Identify the blood parasite species.
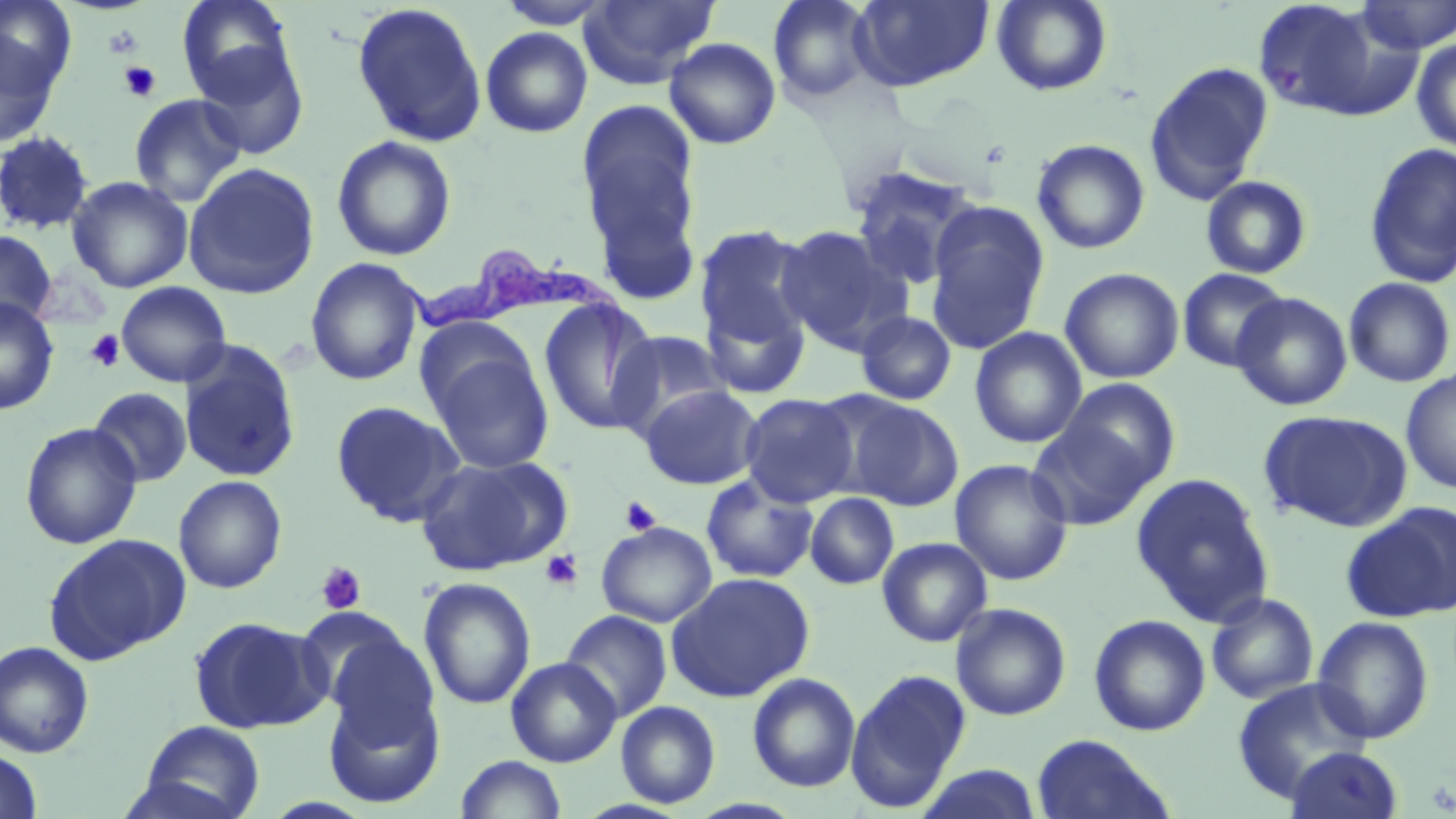
Trypanosoma brucei.

preparation: thin blood film
uninfected_red_blood_cell_locations: 'approximate bounding boxes as named x1/y1/x2/y2 corners in pixels: (x1=0, y1=0, x2=77, y2=95), (x1=177, y1=0, x2=295, y2=101), (x1=496, y1=0, x2=616, y2=28), (x1=579, y1=0, x2=719, y2=89), (x1=768, y1=0, x2=877, y2=104), (x1=850, y1=0, x2=995, y2=92), (x1=991, y1=0, x2=1112, y2=97), (x1=1251, y1=0, x2=1405, y2=122), (x1=1355, y1=0, x2=1456, y2=54), (x1=351, y1=2, x2=488, y2=148), (x1=480, y1=27, x2=593, y2=138), (x1=0, y1=29, x2=61, y2=149), (x1=664, y1=37, x2=781, y2=149), (x1=1411, y1=38, x2=1456, y2=153), (x1=193, y1=42, x2=309, y2=159), (x1=1144, y1=62, x2=1274, y2=204), (x1=128, y1=93, x2=246, y2=207), (x1=575, y1=99, x2=703, y2=273), (x1=0, y1=130, x2=95, y2=236), (x1=331, y1=135, x2=457, y2=262), (x1=1031, y1=139, x2=1150, y2=254), (x1=1363, y1=141, x2=1456, y2=288), (x1=183, y1=163, x2=320, y2=299), (x1=848, y1=165, x2=985, y2=291), (x1=1200, y1=175, x2=1313, y2=279), (x1=66, y1=176, x2=193, y2=293), (x1=924, y1=201, x2=1051, y2=354), (x1=694, y1=222, x2=816, y2=369), (x1=775, y1=224, x2=909, y2=353), (x1=0, y1=230, x2=56, y2=331), (x1=305, y1=257, x2=426, y2=386), (x1=1060, y1=267, x2=1185, y2=384), (x1=1177, y1=268, x2=1289, y2=373), (x1=1343, y1=277, x2=1455, y2=388), (x1=116, y1=281, x2=232, y2=386), (x1=1231, y1=292, x2=1353, y2=411), (x1=0, y1=297, x2=59, y2=415), (x1=537, y1=298, x2=660, y2=436), (x1=856, y1=311, x2=956, y2=406), (x1=970, y1=327, x2=1087, y2=449), (x1=609, y1=330, x2=733, y2=438), (x1=178, y1=340, x2=302, y2=484), (x1=428, y1=348, x2=555, y2=474), (x1=1401, y1=368, x2=1456, y2=493), (x1=1057, y1=379, x2=1180, y2=489), (x1=639, y1=384, x2=763, y2=490), (x1=89, y1=386, x2=193, y2=487), (x1=739, y1=393, x2=859, y2=507), (x1=840, y1=397, x2=964, y2=511), (x1=331, y1=400, x2=465, y2=527), (x1=1258, y1=409, x2=1413, y2=532), (x1=1027, y1=421, x2=1154, y2=531), (x1=20, y1=422, x2=143, y2=549), (x1=415, y1=454, x2=573, y2=576), (x1=950, y1=458, x2=1074, y2=585), (x1=1131, y1=472, x2=1274, y2=626), (x1=700, y1=474, x2=819, y2=584), (x1=172, y1=475, x2=287, y2=594), (x1=805, y1=493, x2=899, y2=590), (x1=1344, y1=502, x2=1456, y2=622), (x1=596, y1=521, x2=718, y2=627), (x1=43, y1=532, x2=191, y2=664), (x1=877, y1=537, x2=992, y2=647), (x1=666, y1=572, x2=814, y2=702), (x1=418, y1=577, x2=537, y2=710), (x1=1206, y1=592, x2=1319, y2=705), (x1=951, y1=603, x2=1071, y2=721), (x1=560, y1=610, x2=673, y2=723), (x1=296, y1=611, x2=428, y2=728), (x1=1088, y1=614, x2=1211, y2=736), (x1=1311, y1=615, x2=1435, y2=744), (x1=188, y1=616, x2=327, y2=733), (x1=0, y1=641, x2=95, y2=758), (x1=506, y1=657, x2=621, y2=768), (x1=322, y1=669, x2=446, y2=810), (x1=845, y1=669, x2=971, y2=811), (x1=747, y1=672, x2=861, y2=792), (x1=1232, y1=678, x2=1373, y2=803), (x1=615, y1=700, x2=721, y2=808), (x1=138, y1=720, x2=265, y2=819), (x1=1031, y1=734, x2=1175, y2=819), (x1=1283, y1=746, x2=1404, y2=819), (x1=0, y1=748, x2=44, y2=817), (x1=455, y1=755, x2=567, y2=819), (x1=914, y1=764, x2=1044, y2=819)'
field_of_view: single
modality: light microscopy
stain: May-Grünwald-Giemsa
magnification: 1000x
platelet_locations: 'approximate bounding boxes as named x1/y1/x2/y2 corners in pixels: (x1=102, y1=23, x2=145, y2=58), (x1=119, y1=60, x2=161, y2=102), (x1=85, y1=330, x2=125, y2=372), (x1=620, y1=496, x2=662, y2=536), (x1=540, y1=550, x2=583, y2=590), (x1=317, y1=562, x2=366, y2=614)'
image_size: 1456×819 pixels
trypanosoma_brucei_locations: 'approximate bounding boxes as named x1/y1/x2/y2 corners in pixels: (x1=398, y1=247, x2=631, y2=399)'